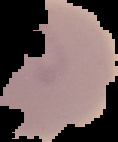
Summary:
  - Malaria status: parasitized
  - Image size: 118×142 pixels
  - Image type: cell region segmented out of the field of view; surrounding area masked to black
  - Preparation: thin blood smear